Describe the morphology of the erythrocytes.
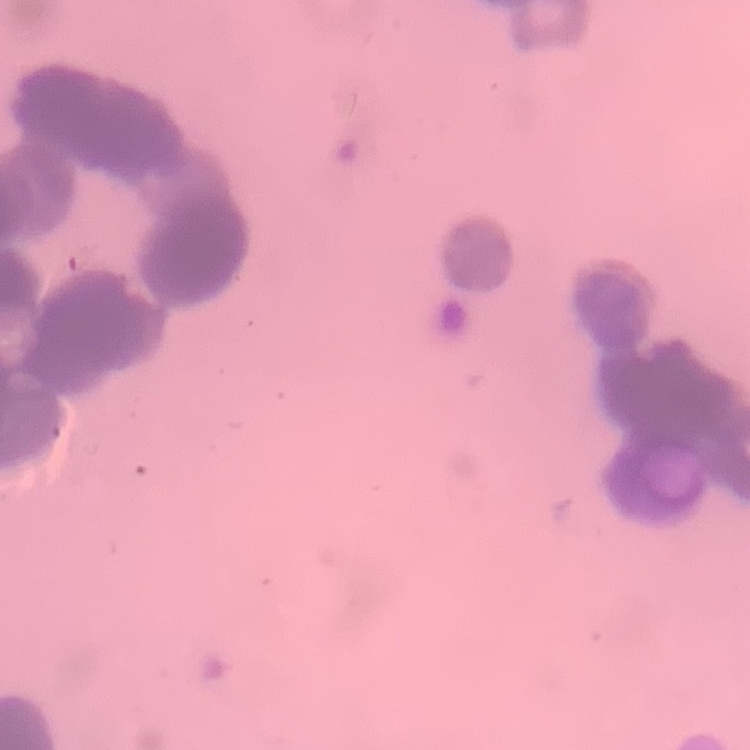
Rouleaux formation.

Thin blood smear. Stained with either Field's or Giemsa. Square crop of a larger photomicrograph.